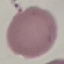

malaria status = uninfected
preparation = thin smear
stain = Giemsa
image type = automatically extracted cell patch, resized to 64 × 64 pixels
capture = smartphone through the microscope eyepiece